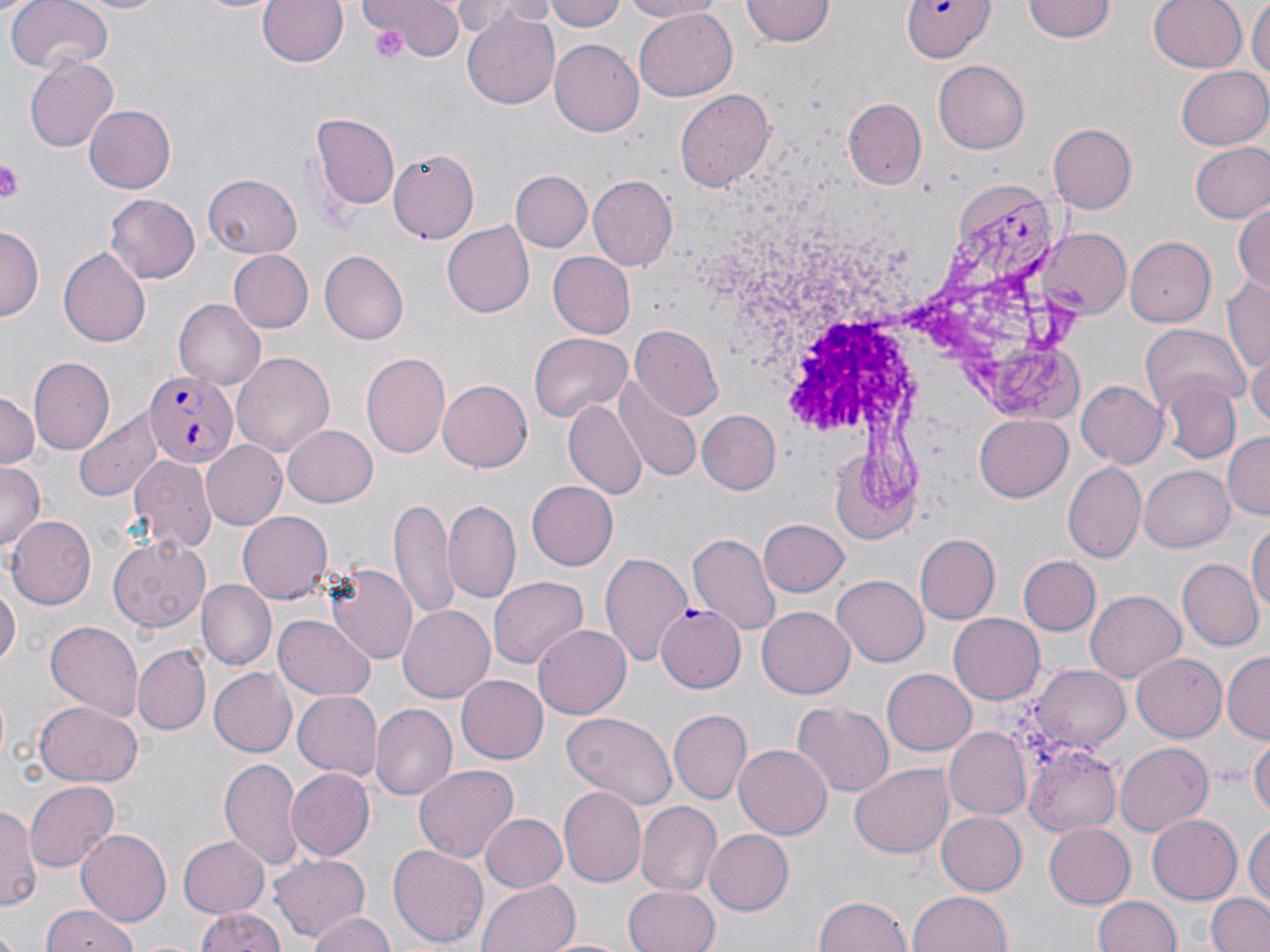

slide-level diagnosis = Plasmodium falciparum
preparation = thin blood smear
stain = May-Grünwald-Giemsa
uninfected red blood cell locations = approximate bounding boxes as (x1, y1, x2, y2) in pixels: (3, 0, 112, 75), (66, 0, 171, 15), (258, 0, 347, 68), (361, 0, 463, 65), (485, 0, 560, 23), (549, 0, 627, 33), (619, 0, 726, 21), (741, 0, 834, 47), (1024, 0, 1115, 43), (1149, 0, 1248, 73), (1248, 0, 1270, 87), (455, 1, 521, 41), (461, 7, 562, 112), (635, 8, 735, 102), (550, 40, 643, 137), (24, 57, 120, 152), (934, 60, 1029, 154), (1177, 66, 1270, 150), (675, 86, 775, 196), (843, 96, 927, 187), (84, 106, 177, 196), (309, 113, 400, 212), (1047, 122, 1135, 214), (1190, 142, 1270, 223), (389, 152, 479, 243), (510, 170, 591, 254), (202, 173, 302, 259), (587, 177, 675, 269), (104, 192, 199, 282), (1234, 199, 1269, 298), (441, 222, 532, 317), (0, 226, 42, 321), (1038, 229, 1130, 319), (1124, 234, 1215, 326), (57, 246, 151, 349), (229, 249, 312, 332), (320, 250, 409, 344), (548, 252, 636, 339), (1223, 276, 1270, 373), (173, 299, 266, 388), (1138, 324, 1247, 406), (630, 326, 722, 420), (529, 332, 629, 423), (231, 351, 336, 459), (1249, 352, 1270, 435), (360, 353, 451, 462), (27, 358, 115, 455), (1156, 376, 1240, 462), (436, 380, 532, 472), (1075, 381, 1167, 469), (615, 382, 701, 482), (0, 390, 40, 468), (565, 398, 647, 497), (74, 406, 165, 501), (695, 408, 781, 495), (975, 412, 1073, 499), (283, 423, 378, 507), (1224, 433, 1270, 520), (200, 441, 289, 530), (822, 446, 920, 550), (129, 456, 216, 549), (1061, 462, 1146, 564), (0, 463, 45, 554), (1140, 466, 1235, 552), (528, 481, 618, 570), (390, 498, 456, 617), (444, 499, 522, 604), (238, 512, 333, 603), (7, 515, 94, 610), (1249, 516, 1270, 626), (758, 517, 850, 598), (690, 532, 782, 637), (914, 534, 1000, 624), (107, 536, 212, 633), (600, 551, 694, 670), (1017, 556, 1100, 636), (1177, 560, 1261, 651), (326, 566, 418, 666), (833, 573, 929, 663), (487, 575, 588, 669), (0, 579, 18, 674), (199, 581, 274, 671), (1086, 588, 1186, 682), (398, 604, 495, 703), (757, 605, 854, 697), (948, 613, 1045, 704), (276, 614, 374, 698), (45, 619, 145, 720), (534, 625, 630, 719), (132, 645, 208, 737), (1133, 652, 1228, 740), (1223, 652, 1270, 741), (1032, 664, 1131, 752), (882, 667, 976, 754), (210, 670, 297, 756), (457, 674, 547, 764), (293, 690, 383, 780), (33, 701, 142, 787), (794, 702, 892, 797), (372, 703, 456, 802), (668, 709, 750, 805), (562, 713, 678, 809), (945, 727, 1031, 820), (1250, 734, 1270, 821), (1021, 741, 1121, 837), (1114, 741, 1214, 837), (735, 744, 831, 840), (219, 757, 307, 872), (413, 764, 518, 863), (850, 764, 952, 859), (285, 769, 374, 861), (24, 780, 119, 870), (559, 786, 648, 887), (0, 801, 37, 910), (636, 803, 719, 897), (480, 812, 569, 893), (935, 812, 1027, 896), (1148, 814, 1242, 902), (1246, 820, 1270, 909), (1042, 822, 1135, 908), (75, 828, 173, 925), (705, 830, 794, 913), (179, 835, 269, 915), (388, 844, 488, 949), (271, 856, 370, 942), (478, 878, 579, 952), (624, 886, 720, 952), (909, 892, 1012, 952), (1207, 893, 1270, 952), (815, 895, 914, 952), (1092, 895, 1180, 952), (38, 905, 140, 952), (193, 909, 286, 952), (304, 912, 398, 952), (549, 936, 629, 952)
Plasmodium falciparum-infected red blood cell locations = approximate bounding boxes as (x1, y1, x2, y2) in pixels: (901, 0, 991, 62), (146, 372, 238, 469), (656, 605, 745, 691)
platelet locations = approximate bounding boxes as (x1, y1, x2, y2) in pixels: (367, 22, 410, 64), (0, 159, 24, 202)
magnification = 1000x
field of view = one of a larger specimen
image size = 1270×952 pixels
modality = light microscopy